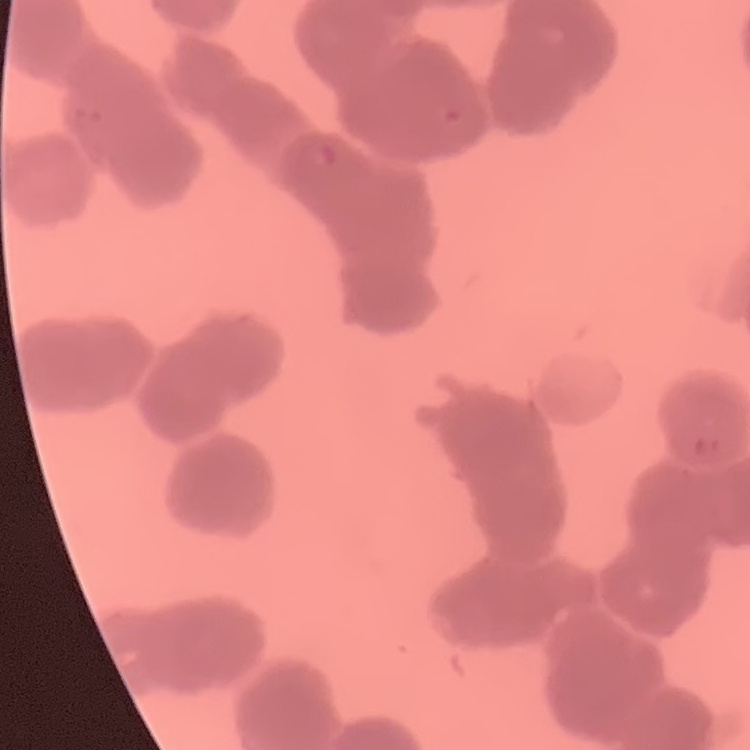

erythrocyte morphology = rouleaux formation
image type = one tile cut from a larger photomicrograph
stain = Field's or Giemsa
preparation = thin blood smear